Assess the morphology of the red blood cells.
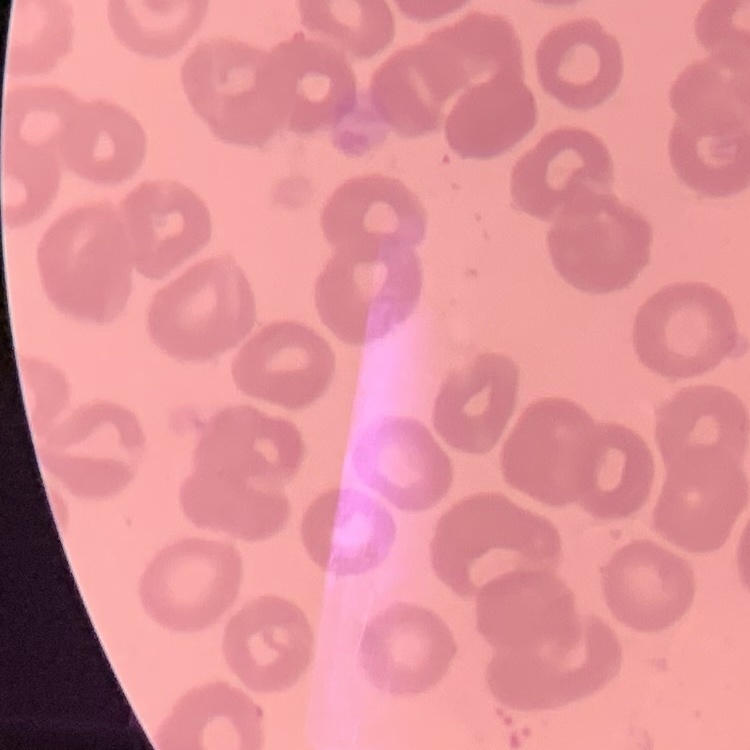

No rouleaux formation.

Field's or Giemsa stain. Thin blood smear. One tile cut from a larger photomicrograph.